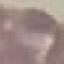

result: negative for malaria parasites
stain: Giemsa
image_type: automatically extracted cell patch, resized to 64 × 64 pixels
capture: smartphone camera at the microscope eyepiece
preparation: thin blood film